Point out each Plasmodium parasite.
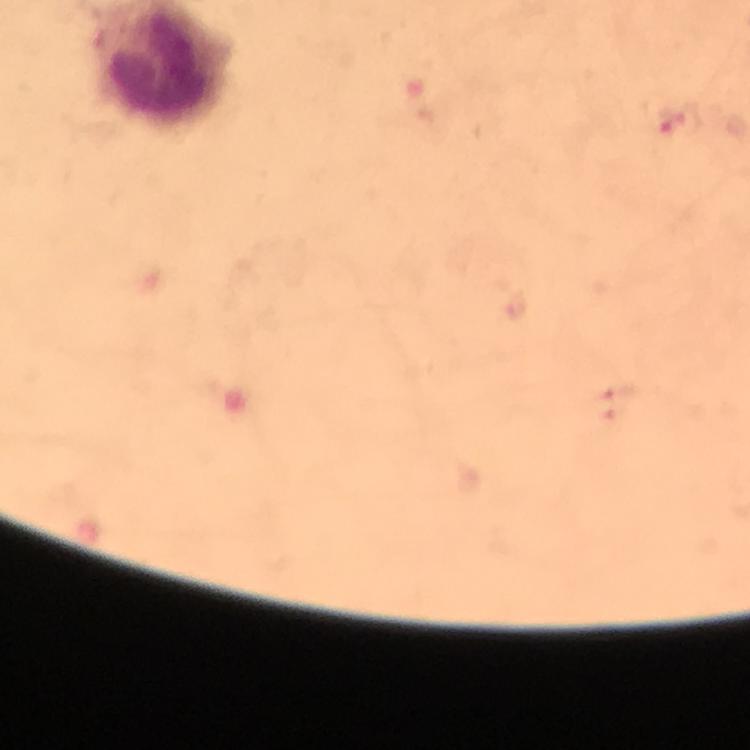

Approximate centers as [x, y] in pixels.
Plasmodium parasites: [683, 120].

From a diagnostic examination for malaria. Photographed through the microscope with a smartphone camera. Immersion oil was used. 100x magnification. Cropped region of a single field of view. Giemsa-stained preparation. Thick blood film. Image is 750×750 pixels.